Describe the morphology of the red blood cells.
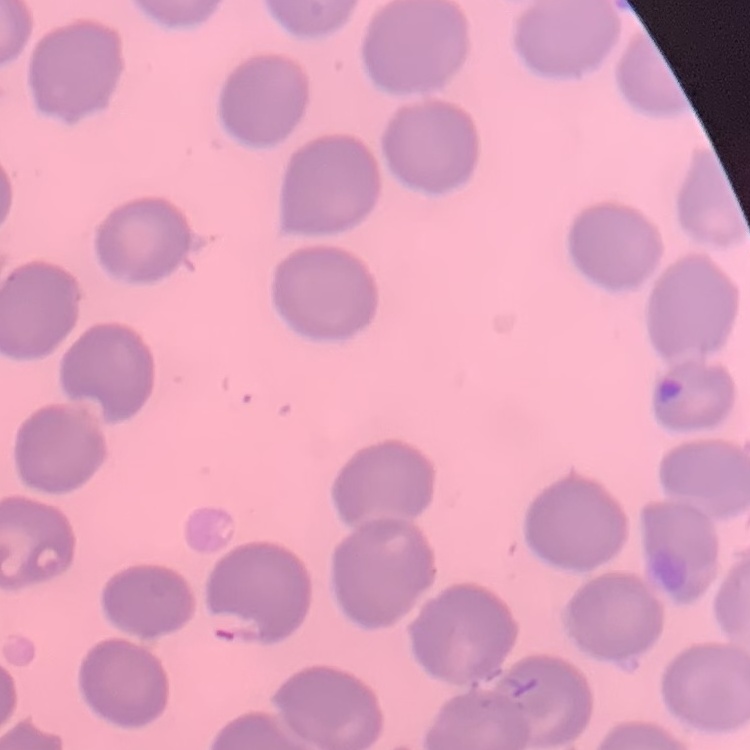
No rouleaux formation.

Summary:
  - Stain: Field's or Giemsa
  - Preparation: thin blood film
  - Image type: one tile cut from a larger photomicrograph